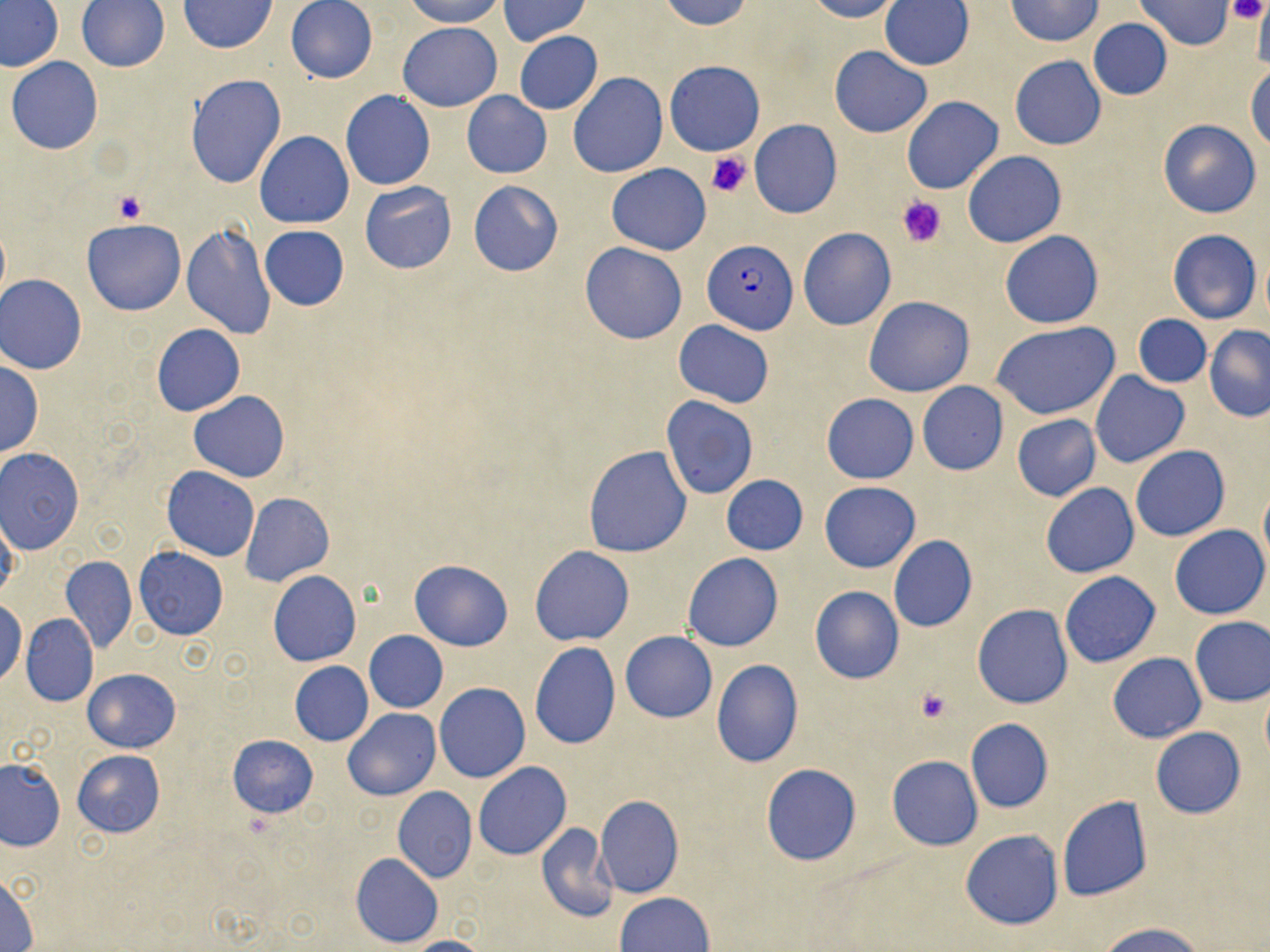
Summary:
  - Coordinate format: approximate bounding boxes as named x1/y1/x2/y2 corners in pixels
  - Plasmodium falciparum-infected red blood cell locations: (x1=702, y1=240, x2=796, y2=334)
  - Uninfected red blood cell locations: (x1=285, y1=0, x2=378, y2=84), (x1=402, y1=0, x2=505, y2=27), (x1=497, y1=0, x2=590, y2=46), (x1=658, y1=0, x2=754, y2=30), (x1=804, y1=0, x2=901, y2=22), (x1=1006, y1=0, x2=1102, y2=46), (x1=1137, y1=0, x2=1232, y2=49), (x1=0, y1=1, x2=66, y2=73), (x1=76, y1=1, x2=170, y2=72), (x1=179, y1=1, x2=276, y2=53), (x1=881, y1=1, x2=973, y2=71), (x1=1252, y1=1, x2=1270, y2=73), (x1=1087, y1=18, x2=1172, y2=100), (x1=398, y1=21, x2=502, y2=112), (x1=514, y1=32, x2=602, y2=114), (x1=829, y1=46, x2=932, y2=138), (x1=1010, y1=55, x2=1106, y2=149), (x1=7, y1=56, x2=104, y2=155), (x1=665, y1=61, x2=764, y2=155), (x1=1246, y1=66, x2=1270, y2=151), (x1=568, y1=73, x2=667, y2=177), (x1=187, y1=74, x2=287, y2=188), (x1=341, y1=91, x2=435, y2=190), (x1=462, y1=91, x2=551, y2=177), (x1=902, y1=97, x2=1003, y2=195), (x1=1158, y1=119, x2=1261, y2=218), (x1=750, y1=121, x2=842, y2=218), (x1=255, y1=131, x2=354, y2=228), (x1=962, y1=151, x2=1066, y2=248), (x1=607, y1=163, x2=711, y2=255), (x1=468, y1=180, x2=563, y2=276), (x1=358, y1=181, x2=457, y2=274), (x1=82, y1=219, x2=186, y2=315), (x1=182, y1=222, x2=277, y2=340), (x1=260, y1=226, x2=349, y2=310), (x1=797, y1=228, x2=895, y2=331), (x1=1168, y1=228, x2=1261, y2=323), (x1=1000, y1=231, x2=1103, y2=329), (x1=579, y1=242, x2=688, y2=344), (x1=1, y1=274, x2=87, y2=374), (x1=863, y1=296, x2=974, y2=397), (x1=1133, y1=314, x2=1211, y2=388), (x1=674, y1=320, x2=773, y2=408), (x1=993, y1=322, x2=1119, y2=420), (x1=151, y1=324, x2=246, y2=415), (x1=1205, y1=325, x2=1270, y2=422), (x1=0, y1=359, x2=43, y2=459), (x1=1090, y1=371, x2=1189, y2=468), (x1=917, y1=382, x2=1007, y2=474), (x1=189, y1=392, x2=290, y2=482), (x1=821, y1=394, x2=918, y2=484), (x1=662, y1=396, x2=758, y2=498), (x1=612, y1=411, x2=754, y2=529), (x1=1012, y1=414, x2=1101, y2=502), (x1=584, y1=445, x2=692, y2=557), (x1=1131, y1=445, x2=1228, y2=542), (x1=1, y1=448, x2=86, y2=553), (x1=161, y1=465, x2=260, y2=561), (x1=721, y1=475, x2=808, y2=555), (x1=819, y1=481, x2=921, y2=573), (x1=1259, y1=482, x2=1270, y2=571), (x1=1041, y1=483, x2=1139, y2=578), (x1=239, y1=492, x2=334, y2=586), (x1=0, y1=511, x2=18, y2=603), (x1=1171, y1=524, x2=1269, y2=620), (x1=888, y1=536, x2=978, y2=633), (x1=134, y1=546, x2=227, y2=640), (x1=530, y1=546, x2=634, y2=646), (x1=682, y1=553, x2=783, y2=652), (x1=61, y1=556, x2=137, y2=653), (x1=409, y1=559, x2=513, y2=651), (x1=268, y1=571, x2=361, y2=667), (x1=1059, y1=571, x2=1160, y2=668), (x1=808, y1=588, x2=904, y2=683), (x1=0, y1=599, x2=26, y2=687), (x1=972, y1=604, x2=1073, y2=709), (x1=21, y1=613, x2=98, y2=708), (x1=1190, y1=617, x2=1270, y2=706), (x1=365, y1=631, x2=448, y2=713), (x1=620, y1=631, x2=716, y2=723), (x1=529, y1=642, x2=621, y2=750), (x1=1107, y1=653, x2=1206, y2=743), (x1=711, y1=659, x2=803, y2=766), (x1=289, y1=661, x2=373, y2=746), (x1=83, y1=668, x2=180, y2=752), (x1=434, y1=683, x2=530, y2=783), (x1=1260, y1=687, x2=1270, y2=765), (x1=343, y1=707, x2=441, y2=800), (x1=965, y1=719, x2=1053, y2=813), (x1=1149, y1=727, x2=1246, y2=819), (x1=227, y1=734, x2=318, y2=817), (x1=72, y1=750, x2=165, y2=836), (x1=886, y1=755, x2=983, y2=851), (x1=0, y1=759, x2=65, y2=851), (x1=474, y1=762, x2=572, y2=860), (x1=761, y1=764, x2=862, y2=865), (x1=393, y1=787, x2=477, y2=882), (x1=596, y1=794, x2=683, y2=898), (x1=1057, y1=795, x2=1152, y2=902), (x1=534, y1=821, x2=618, y2=924), (x1=960, y1=830, x2=1063, y2=930), (x1=351, y1=853, x2=443, y2=949), (x1=1, y1=873, x2=38, y2=952), (x1=616, y1=892, x2=714, y2=952), (x1=1102, y1=922, x2=1206, y2=952), (x1=400, y1=936, x2=490, y2=952)
  - Platelet locations: (x1=1229, y1=0, x2=1267, y2=25), (x1=707, y1=149, x2=753, y2=199), (x1=113, y1=190, x2=148, y2=225), (x1=897, y1=195, x2=946, y2=247), (x1=914, y1=687, x2=952, y2=723), (x1=239, y1=812, x2=279, y2=842)
  - Slide-level diagnosis: Plasmodium falciparum
  - Modality: optical microscopy
  - Field of view: one of a larger specimen
  - Stain: May-Grünwald-Giemsa
  - Preparation: thin blood film
  - Magnification: 1000x
  - Image size: 1270×952 pixels